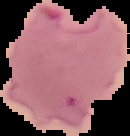
The area outside the segmented cell region is set to black. Malaria status: parasitized. From a thin blood film. Image is 130×136 pixels.